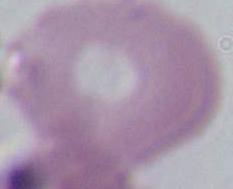

magnification = 1000x
identification = red blood cell
modality = micrograph